State which cell type is depicted.
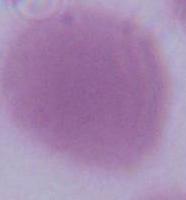
An erythrocyte.

Summary:
  - Modality: micrograph
  - Magnification: 1000x